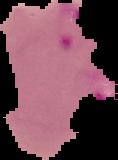

image size = 118×160 pixels
preparation = thin blood smear
malaria status = parasitized
image type = segmented cell region with the area outside set to black